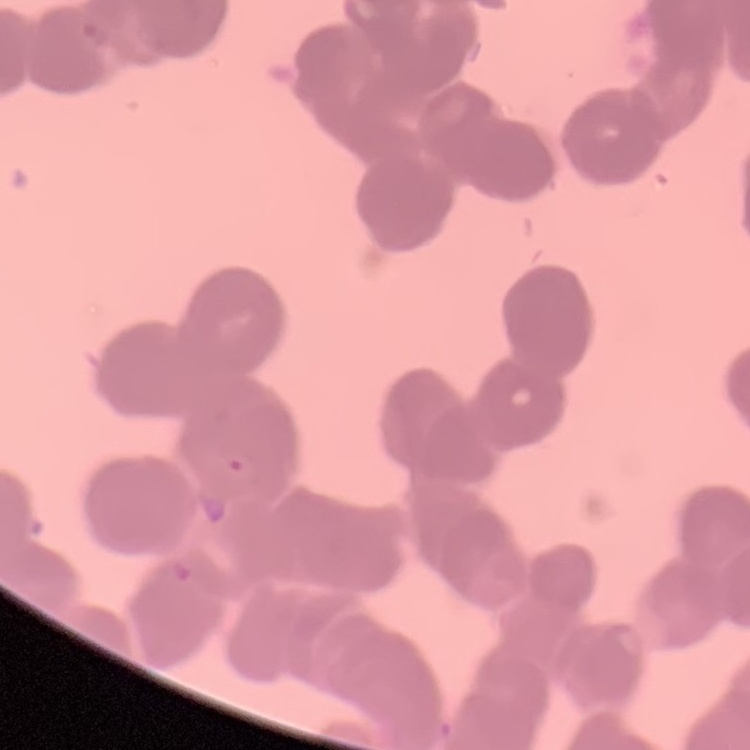
erythrocyte_morphology: rouleaux formation
stain: Field's or Giemsa
image_type: one tile cut from a larger photomicrograph
preparation: thin peripheral smear